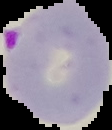
image type = cell region segmented out of the field of view; surrounding area masked to black
preparation = thin blood film
image size = 112×130 pixels
malaria status = parasitized